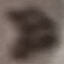

Summary:
  - Malaria status: uninfected
  - Preparation: thin blood film
  - Image type: cell patch, automatically extracted from a larger field of view and resized to 64 × 64 pixels
  - Capture: smartphone through the microscope eyepiece
  - Stain: Giemsa